Give the position of every Plasmodium parasite.
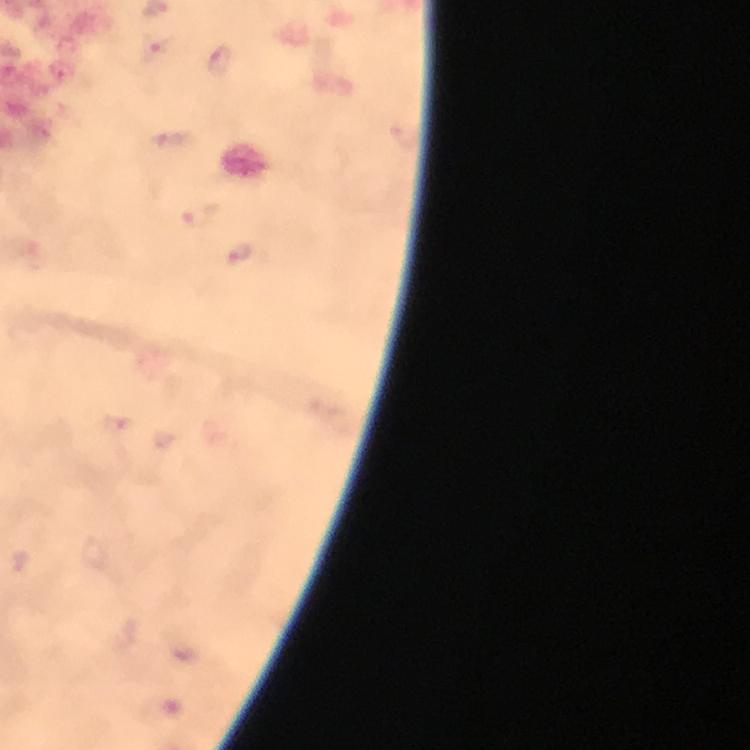
Approximate centers as {x, y} in pixels.
Plasmodium parasites: {158, 47}, {219, 60}, {170, 138}, {200, 215}, {240, 254}.

cropped_from: one field of view
preparation: thick blood film
magnification: 100x
image_size: 750×750 pixels
capture: smartphone mounted on the microscope
context: from a diagnostic examination for malaria
immersion_oil: used
stain: Giemsa